Outline each white blood cell.
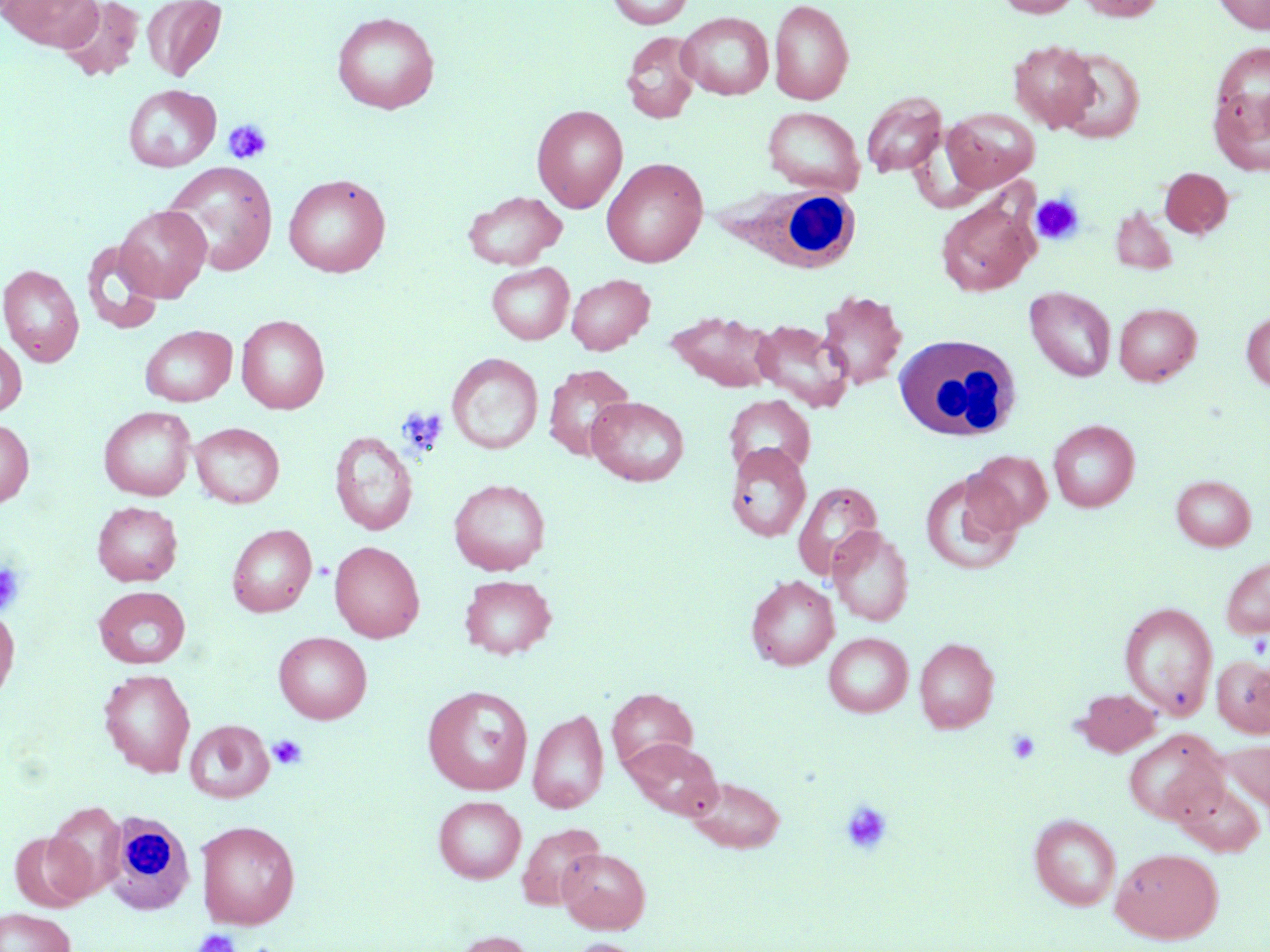

Approximate bounding boxes as [x1, y1, x2, y2] in pixels.
White blood cells: [711, 183, 865, 275], [893, 333, 1022, 442], [99, 811, 199, 915].

Summary:
  - Platelet locations: [223, 120, 272, 164], [1030, 193, 1084, 246], [396, 406, 448, 457], [0, 562, 25, 615], [1006, 729, 1041, 764], [268, 735, 307, 771], [840, 800, 893, 855], [192, 929, 241, 952]
  - Uninfected red blood cell locations: [1, 0, 103, 51], [57, 0, 145, 82], [606, 0, 694, 29], [769, 0, 854, 105], [996, 0, 1081, 17], [1075, 0, 1165, 21], [1212, 0, 1270, 34], [141, 1, 227, 81], [331, 11, 440, 114], [677, 12, 774, 100], [621, 30, 702, 124], [1008, 40, 1100, 132], [1212, 42, 1270, 129], [1055, 49, 1145, 143], [123, 84, 221, 172], [1209, 86, 1270, 177], [861, 91, 947, 177], [532, 104, 628, 212], [763, 107, 864, 195], [942, 107, 1040, 192], [601, 157, 708, 267], [162, 162, 278, 276], [1159, 167, 1232, 238], [283, 173, 391, 277], [462, 191, 566, 270], [936, 198, 1038, 297], [114, 204, 212, 302], [1110, 204, 1178, 275], [82, 241, 163, 335], [486, 262, 574, 344], [0, 264, 84, 366], [567, 273, 654, 355], [1025, 286, 1117, 381], [816, 290, 907, 391], [1114, 302, 1201, 386], [667, 309, 778, 392], [1241, 311, 1270, 391], [236, 314, 330, 413], [750, 320, 853, 412], [140, 325, 237, 406], [0, 335, 26, 416], [447, 352, 543, 454], [544, 364, 635, 460], [723, 394, 815, 478], [587, 396, 689, 486], [99, 406, 196, 500], [0, 418, 34, 508], [1048, 419, 1139, 512], [190, 422, 284, 508], [329, 431, 417, 535], [725, 443, 812, 541], [967, 450, 1052, 533], [920, 471, 1023, 576], [1171, 475, 1256, 551], [449, 478, 550, 576], [792, 481, 882, 580], [93, 501, 182, 586], [227, 524, 316, 616], [828, 526, 914, 626], [329, 541, 424, 642], [1221, 555, 1270, 639], [459, 574, 557, 659], [746, 575, 839, 670], [94, 586, 190, 669], [1119, 601, 1218, 720], [0, 605, 19, 705], [274, 632, 371, 724], [824, 633, 913, 717], [915, 637, 999, 733], [1212, 655, 1270, 737], [99, 669, 195, 777], [422, 686, 533, 796], [607, 687, 698, 773], [1074, 688, 1161, 756], [527, 709, 609, 814], [186, 720, 273, 803], [1123, 729, 1227, 825], [623, 737, 722, 819], [1223, 738, 1270, 816], [686, 776, 785, 853], [1174, 779, 1266, 857], [433, 795, 526, 883], [44, 802, 126, 900], [1029, 813, 1121, 910], [196, 820, 300, 929], [517, 823, 605, 910], [10, 831, 93, 912], [558, 847, 649, 933], [1111, 847, 1223, 943], [0, 908, 75, 952], [448, 930, 537, 952], [567, 939, 645, 952]
  - Slide-level diagnosis: no evidence of blood parasites
  - Modality: optical microscopy
  - Image size: 1270×952 pixels
  - Preparation: thin blood smear
  - Stain: May-Grünwald-Giemsa
  - Magnification: 1000x
  - Field of view: single